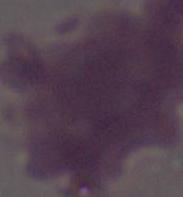 A red blood cell is seen. Photomicrograph. 1000x magnification.